Name the blood parasite species.
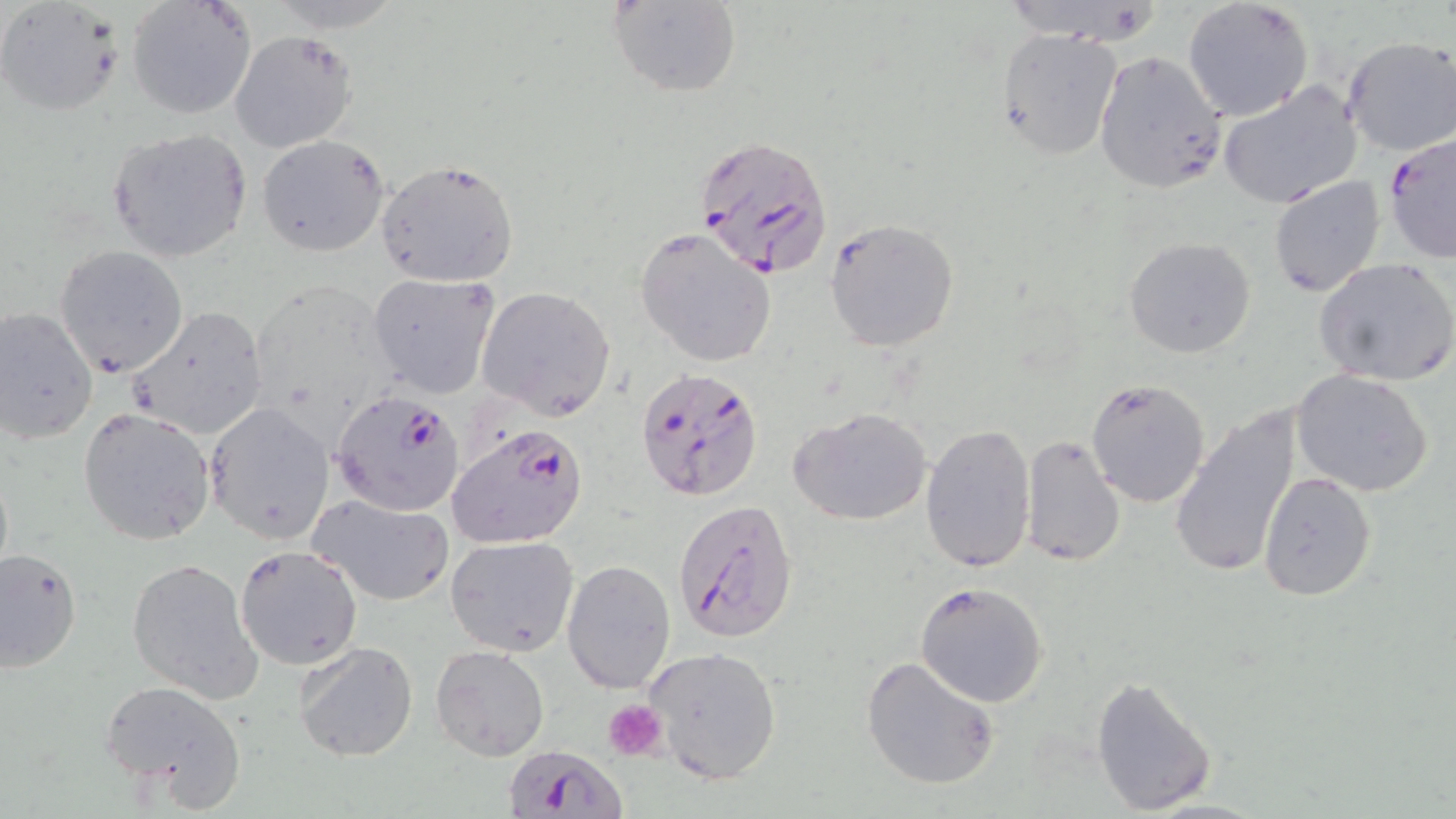
Plasmodium falciparum.

Approximate bounding boxes as named x1/y1/x2/y2 corners in pixels. Uninfected red blood cell locations: (x1=606, y1=0, x2=742, y2=98), (x1=125, y1=1, x2=256, y2=121), (x1=1182, y1=1, x2=1314, y2=122), (x1=1, y1=3, x2=122, y2=115), (x1=995, y1=26, x2=1123, y2=160), (x1=230, y1=32, x2=358, y2=152), (x1=1339, y1=35, x2=1456, y2=158), (x1=1093, y1=50, x2=1227, y2=194), (x1=1218, y1=82, x2=1363, y2=209), (x1=106, y1=128, x2=253, y2=263), (x1=256, y1=134, x2=390, y2=257), (x1=373, y1=156, x2=520, y2=288), (x1=1268, y1=175, x2=1386, y2=298), (x1=825, y1=219, x2=959, y2=352), (x1=636, y1=228, x2=775, y2=368), (x1=1123, y1=236, x2=1256, y2=358), (x1=54, y1=245, x2=188, y2=377), (x1=1314, y1=257, x2=1456, y2=386), (x1=367, y1=273, x2=498, y2=397), (x1=478, y1=286, x2=617, y2=418), (x1=0, y1=306, x2=98, y2=443), (x1=128, y1=307, x2=269, y2=441), (x1=1292, y1=370, x2=1434, y2=498), (x1=1085, y1=375, x2=1212, y2=506), (x1=204, y1=400, x2=335, y2=545), (x1=1169, y1=406, x2=1304, y2=580), (x1=78, y1=407, x2=219, y2=546), (x1=791, y1=408, x2=933, y2=526), (x1=919, y1=422, x2=1036, y2=572), (x1=1020, y1=436, x2=1125, y2=567), (x1=1258, y1=471, x2=1377, y2=600), (x1=308, y1=495, x2=457, y2=605), (x1=446, y1=536, x2=578, y2=657), (x1=234, y1=545, x2=362, y2=670), (x1=0, y1=546, x2=83, y2=672), (x1=126, y1=558, x2=263, y2=701), (x1=562, y1=560, x2=675, y2=694), (x1=914, y1=582, x2=1049, y2=707), (x1=294, y1=640, x2=419, y2=763), (x1=431, y1=644, x2=550, y2=760), (x1=644, y1=645, x2=783, y2=783), (x1=862, y1=656, x2=1002, y2=790), (x1=1090, y1=674, x2=1217, y2=816), (x1=98, y1=679, x2=246, y2=803). Platelet locations: (x1=605, y1=700, x2=669, y2=762). Plasmodium falciparum-infected red blood cell locations: (x1=695, y1=133, x2=836, y2=279), (x1=1383, y1=134, x2=1455, y2=267), (x1=635, y1=364, x2=764, y2=503), (x1=329, y1=389, x2=466, y2=515), (x1=445, y1=422, x2=589, y2=551), (x1=671, y1=497, x2=800, y2=644), (x1=507, y1=743, x2=624, y2=818). Single field of view. Light microscopy. Image is 1456×819 pixels. Thin blood smear. May-Grünwald-Giemsa-stained preparation. Captured at 1000x magnification.